Classify this cell by malaria status.
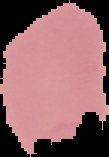

Uninfected.

image size = 109×157 pixels
preparation = thin blood film
image type = segmented cell region on a black background